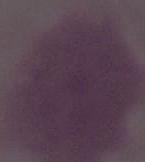
{
  "magnification": "1000x",
  "modality": "photomicrograph",
  "identification": "erythrocyte"
}